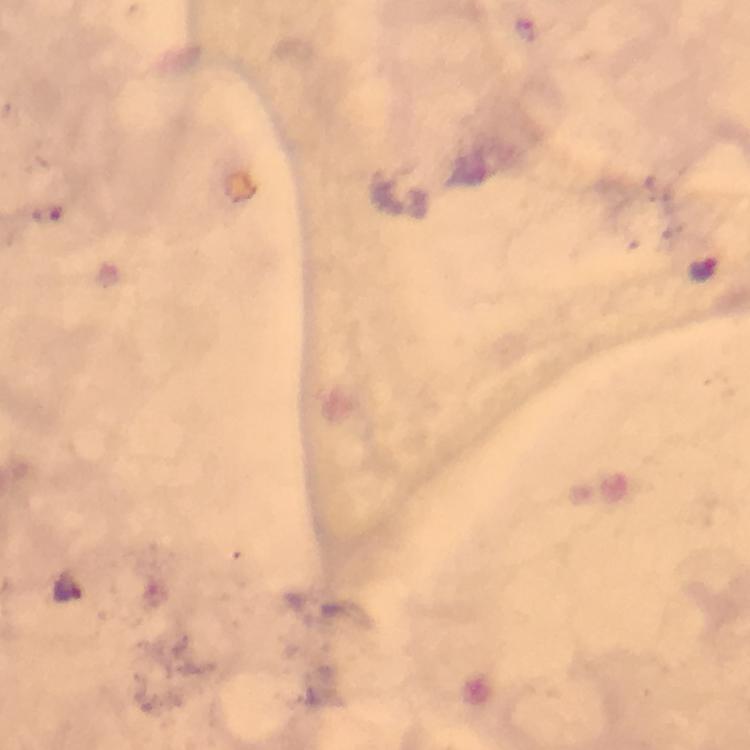
magnification = 100x
Plasmodium parasite locations = approximate centers as [x, y] in pixels: [702, 267], [66, 583]
image size = 750×750 pixels
preparation = thick smear
stain = Giemsa
capture = smartphone photograph through a microscope
context = from a diagnostic examination for malaria
cropped from = one field of view
immersion oil = applied